Report the malaria status of this cell.
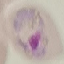
Parasitized.

preparation: thin blood film
capture: smartphone camera at the microscope eyepiece
stain: Giemsa
image_type: automatically extracted cell patch, resized to 64 × 64 pixels